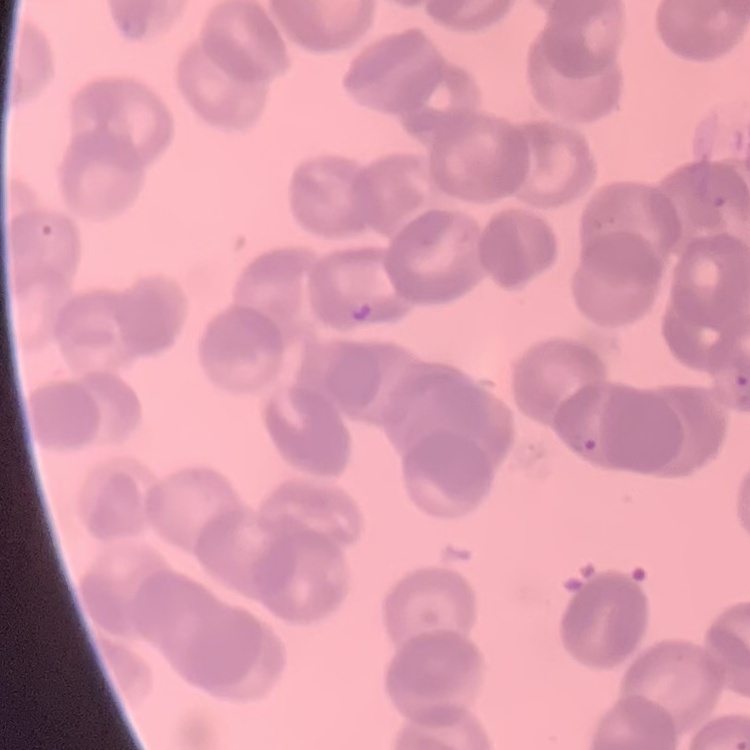
{
  "red_blood_cell_morphology": "rouleaux formation",
  "preparation": "thin blood smear",
  "image_type": "square crop of a larger photomicrograph",
  "stain": "Field's or Giemsa"
}